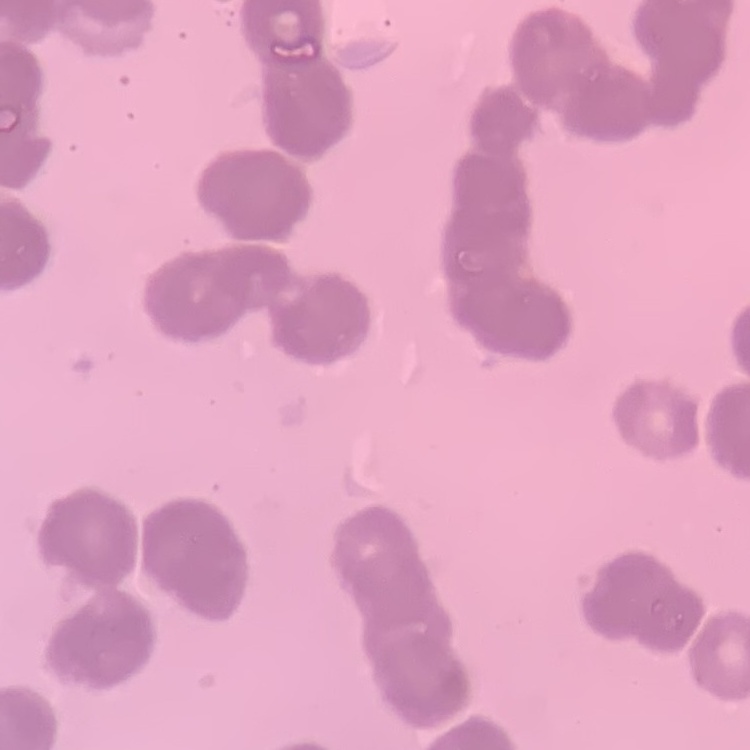

Summary:
  - Erythrocyte morphology: rouleaux formation
  - Stain: Field's or Giemsa
  - Image type: one tile cut from a larger photomicrograph
  - Preparation: thin blood smear